State which parasite is depicted.
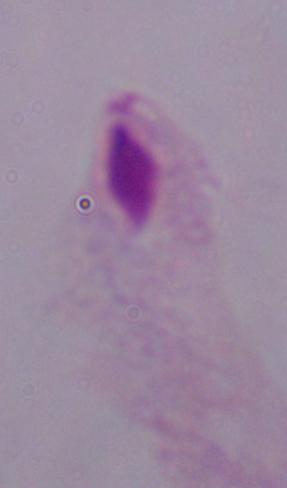
A trichomonad.

magnification = 1000x
modality = micrograph